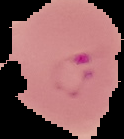

image size = 124×139 pixels
preparation = thin blood smear
malaria status = parasitized
image type = segmented cell region with the area outside set to black